Locate every malaria parasite.
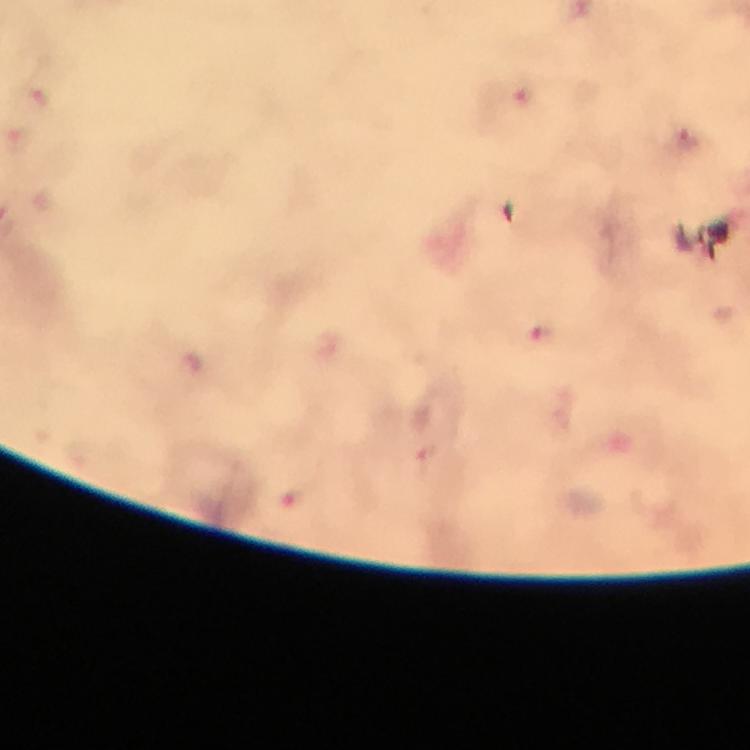

Approximate centers as (x, y) in pixels.
Malaria parasites: (523, 95), (685, 139), (540, 338), (426, 459).

Immersion oil was used. Image is 750×750 pixels. At 100x magnification. Giemsa stain. Photographed with a smartphone mounted on the microscope. A crop from one field of view. From a diagnostic examination for malaria. Thick blood smear.